Mark where leukocytes are.
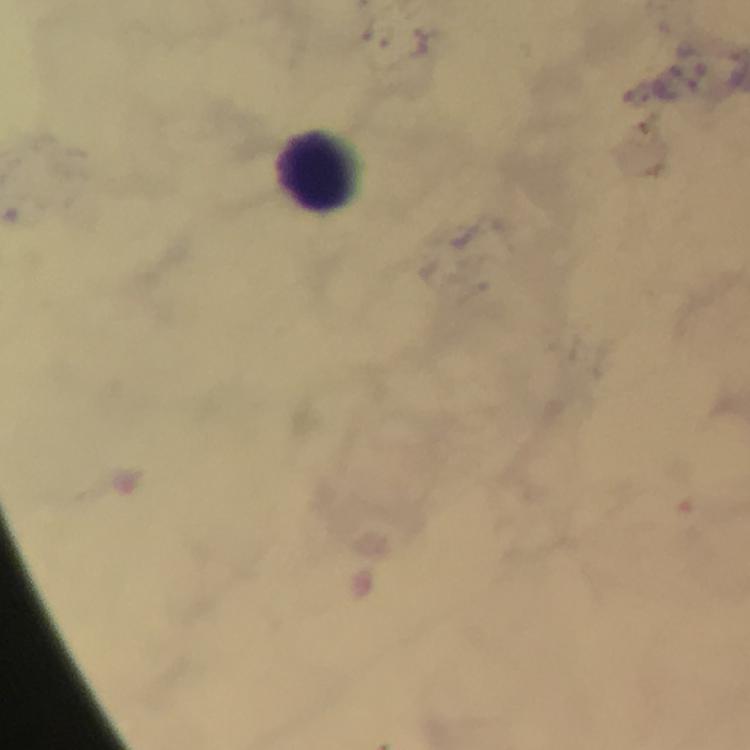
Approximate centers as (x, y) in pixels.
Leukocytes: (324, 169).

Thick blood smear. From a malaria diagnostic workup. Giemsa stain. Photographed through the microscope with a smartphone camera. Image is 750×750 pixels. At 100x magnification. Cropped region of a single field of view. Immersion oil was used. Malaria parasites: none seen.